Locate every Plasmodium parasite.
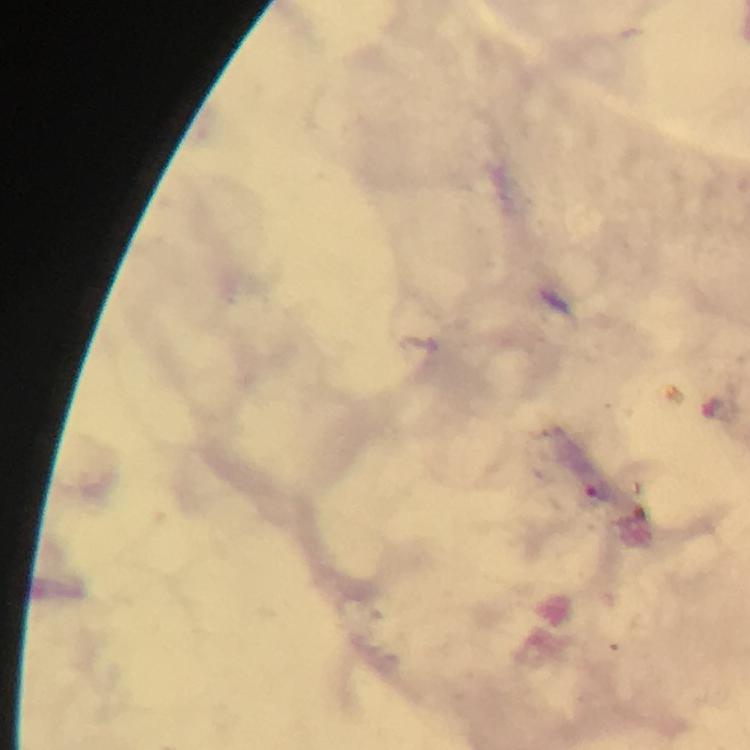

Approximate object centers, in pixels from the top-left corner.
Plasmodium parasites: (x=599, y=490).

Summary:
  - Image size: 750×750 pixels
  - Magnification: 100x
  - Stain: Giemsa
  - Immersion oil: used
  - Capture: smartphone camera through the microscope
  - Preparation: thick smear
  - Context: from a malaria diagnostic workup
  - Cropped from: one field of view